Locate every blood parasite and identify its species.
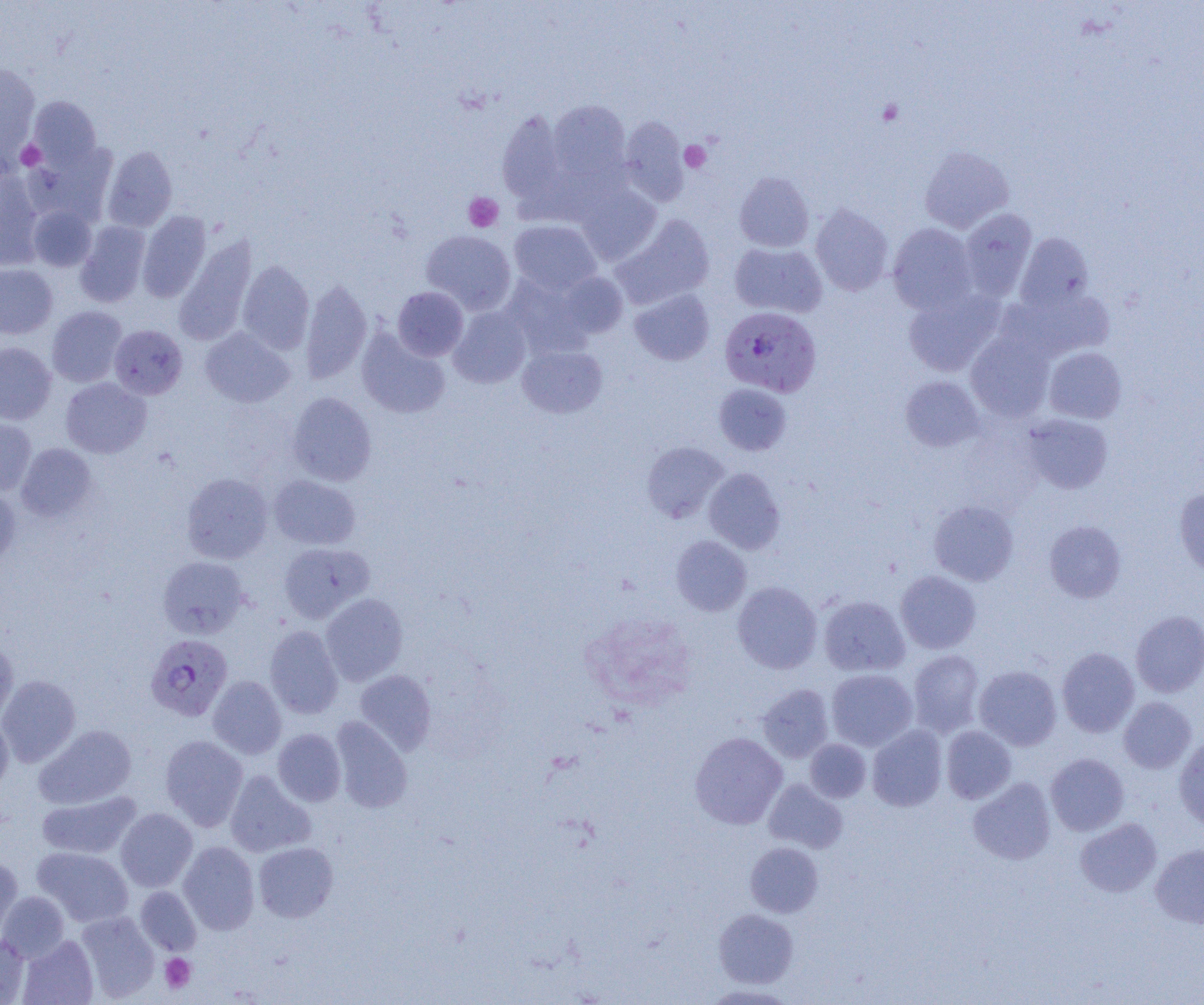

Approximate bounding boxes as (x1, y1, x2, y2) in pixels.
Plasmodium falciparum-infected red blood cells: (719, 305, 821, 397), (146, 634, 233, 721).
No Plasmodium ovale, Plasmodium malariae, Plasmodium vivax, Babesia divergens, or Trypanosoma brucei observed.

Uninfected red blood cell locations: (0, 62, 41, 167), (28, 96, 102, 170), (548, 100, 630, 183), (496, 108, 568, 209), (619, 116, 689, 204), (24, 143, 117, 227), (103, 146, 177, 232), (919, 146, 1014, 233), (0, 169, 44, 269), (734, 172, 814, 252), (576, 183, 662, 264), (28, 205, 97, 271), (811, 205, 893, 295), (959, 209, 1037, 300), (137, 210, 211, 302), (613, 214, 714, 309), (509, 220, 601, 295), (75, 221, 150, 307), (888, 223, 977, 314), (421, 230, 516, 315), (1015, 233, 1094, 311), (175, 237, 258, 344), (729, 242, 827, 318), (238, 260, 314, 354), (0, 263, 57, 339), (557, 272, 628, 339), (502, 273, 596, 358), (300, 278, 372, 384), (392, 287, 469, 361), (630, 288, 714, 365), (903, 288, 1004, 377), (1006, 290, 1115, 362), (47, 306, 126, 387), (449, 306, 531, 388), (109, 324, 187, 399), (200, 328, 294, 408), (356, 329, 450, 419), (966, 331, 1054, 422), (0, 342, 56, 424), (517, 345, 607, 418), (1044, 347, 1127, 423), (901, 376, 984, 452), (61, 378, 151, 458), (714, 383, 791, 455), (287, 391, 377, 486), (1022, 414, 1114, 494), (0, 417, 36, 496), (641, 441, 728, 522), (16, 443, 97, 522), (704, 468, 785, 554), (181, 472, 273, 564), (268, 475, 361, 550), (0, 486, 20, 568), (1174, 487, 1204, 577), (929, 500, 1018, 585), (1044, 520, 1125, 603), (671, 535, 751, 616), (278, 542, 373, 623), (157, 556, 249, 638), (896, 571, 981, 654), (733, 581, 822, 673), (320, 593, 408, 685), (819, 596, 909, 677), (1131, 610, 1204, 697), (265, 625, 343, 718), (0, 642, 18, 722), (1057, 647, 1139, 737), (908, 650, 984, 737), (974, 665, 1061, 750), (355, 669, 436, 754), (827, 669, 918, 751), (0, 675, 81, 767), (208, 675, 287, 759), (757, 684, 834, 762), (1118, 697, 1197, 774), (0, 713, 13, 795), (330, 717, 412, 813), (34, 724, 136, 809), (867, 725, 947, 811), (941, 726, 1016, 803), (273, 729, 346, 806), (689, 732, 787, 829), (160, 735, 249, 830), (1174, 735, 1204, 832), (805, 739, 871, 802), (1046, 753, 1129, 836), (225, 770, 316, 857), (968, 777, 1056, 865), (764, 779, 847, 853), (37, 790, 141, 859), (115, 807, 197, 892), (1075, 818, 1161, 897), (178, 841, 259, 934), (253, 842, 338, 922), (745, 842, 823, 917), (1150, 843, 1204, 928), (33, 847, 133, 927), (0, 856, 23, 941), (135, 886, 201, 956), (0, 891, 70, 963), (714, 908, 799, 988), (76, 910, 159, 1001), (0, 932, 29, 1004), (18, 935, 98, 1005), (700, 983, 800, 1004). Platelet locations: (877, 99, 903, 125), (16, 140, 46, 170), (680, 141, 711, 172), (463, 192, 503, 232), (160, 953, 196, 993). Slide-level diagnosis: Plasmodium falciparum. Light microscopy. One field of a larger specimen. Image is 1204×1005 pixels. Thin blood film. Captured at 1000x magnification.